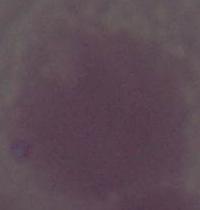
Captured at 1000x magnification. Photomicrograph. A red blood cell is seen.